Assess this cell for malaria.
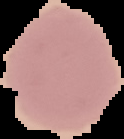
It is uninfected.

Image is 124×139 pixels. From a thin blood film. Cell region segmented out of the field of view; the surrounding area is masked to black.